Classify this cell by malaria status.
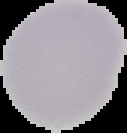
It is uninfected.

Summary:
  - Image size: 127×133 pixels
  - Preparation: thin blood film
  - Image type: cell region segmented out of the field of view; surrounding area masked to black